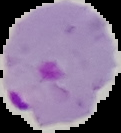

Summary:
  - Result: Plasmodium parasites detected
  - Image size: 121×133 pixels
  - Image type: segmented cell region with the area outside set to black
  - Preparation: thin blood film